Give the preparation type.
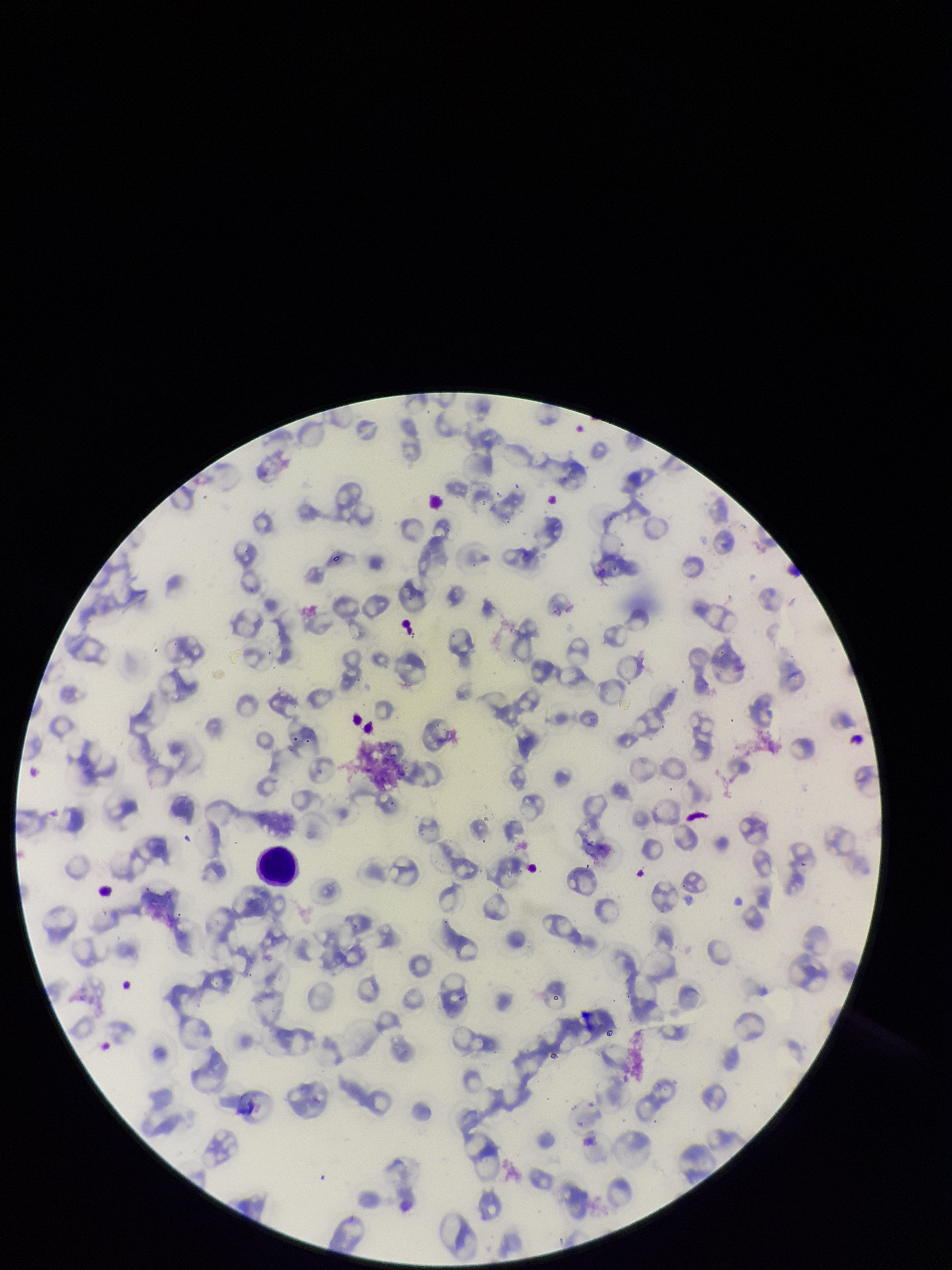

Thin.

species reported for this patient = Plasmodium falciparum
capture = smartphone photograph through the microscope eyepiece
parasitized red blood cells = none seen
red blood cell count = 83
field of view = one from this slide
image size = 952×1270 pixels
stain = Giemsa
parasitized red blood cell count = 0
patient malaria status = positive